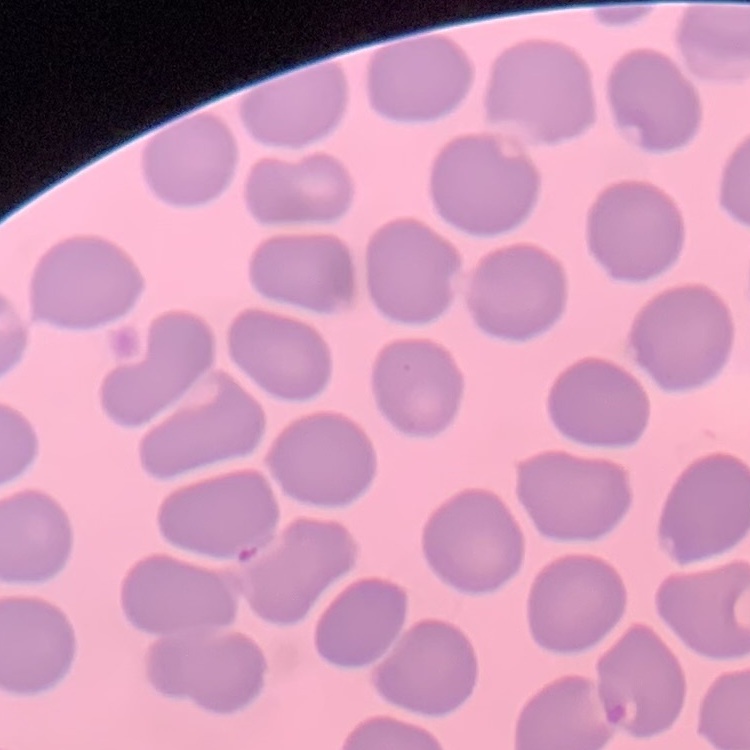

erythrocyte morphology = no rouleaux formation
preparation = thin blood smear
stain = Field's or Giemsa
image type = square crop of a larger photomicrograph